Comment on the morphology of the red blood cells.
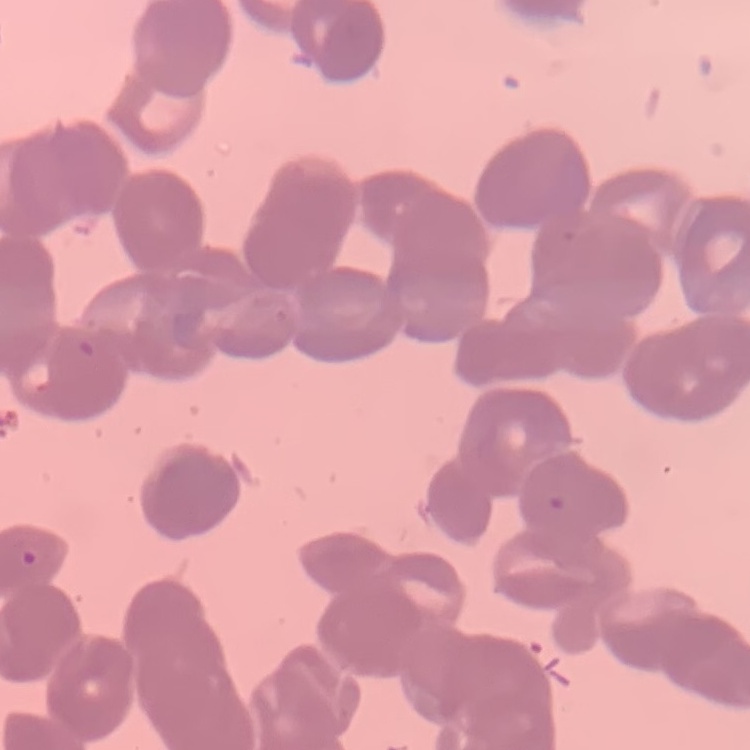
Rouleaux formation.

image_type: one tile cut from a larger photomicrograph
stain: Field's or Giemsa
preparation: thin blood smear